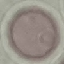
malaria status = uninfected
preparation = thin blood smear
image type = automatically extracted cell patch, resized to 64 × 64 pixels
stain = Giemsa
capture = smartphone camera at the microscope eyepiece